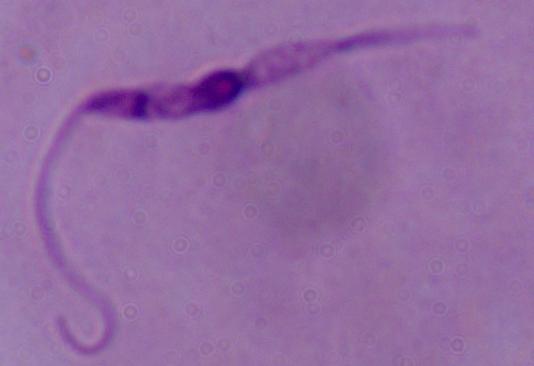

Photomicrograph. 1000x magnification. A Leishmania parasite is shown.